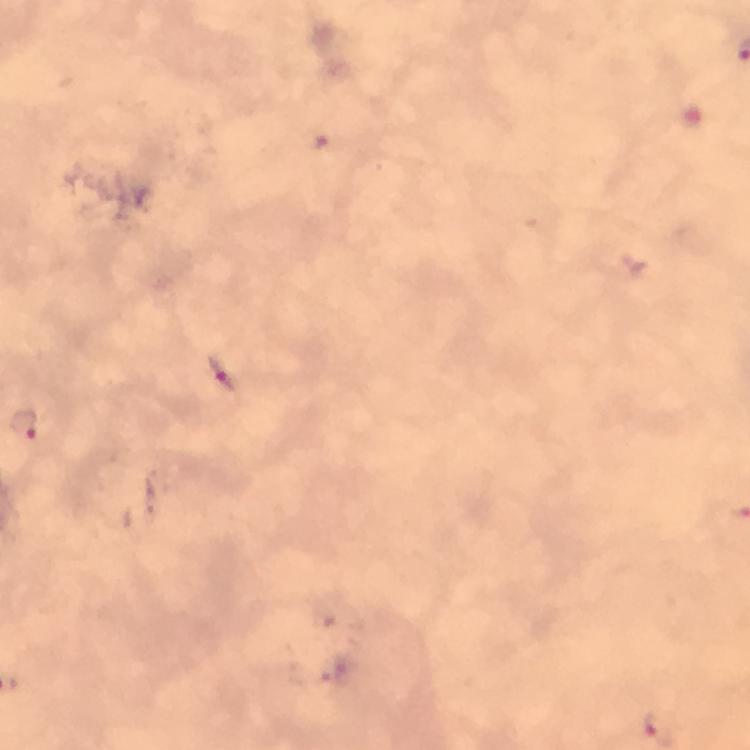

Approximate centers as {x, y} in pixels. Malaria parasite locations: {220, 375}, {26, 422}. Thick blood film. Giemsa-stained preparation. 100x magnification. Image is 750×750 pixels. Immersion oil applied. A crop from one field of view. From a diagnostic examination for malaria. Photographed with a smartphone mounted on the microscope.